Assess the morphology of the red blood cells.
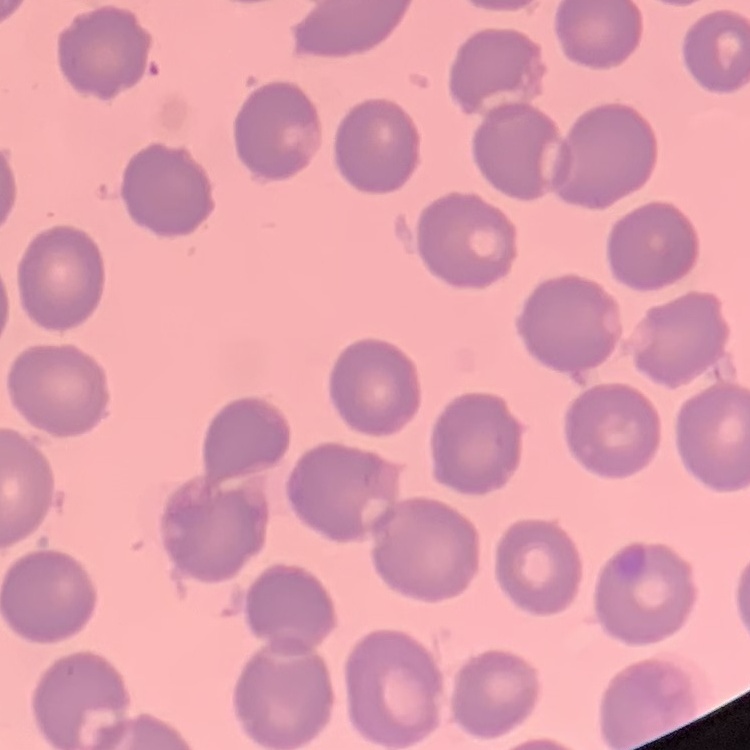
They show no rouleaux formation.

Summary:
  - Preparation: thin peripheral smear
  - Stain: Field's or Giemsa
  - Image type: square crop of a larger photomicrograph